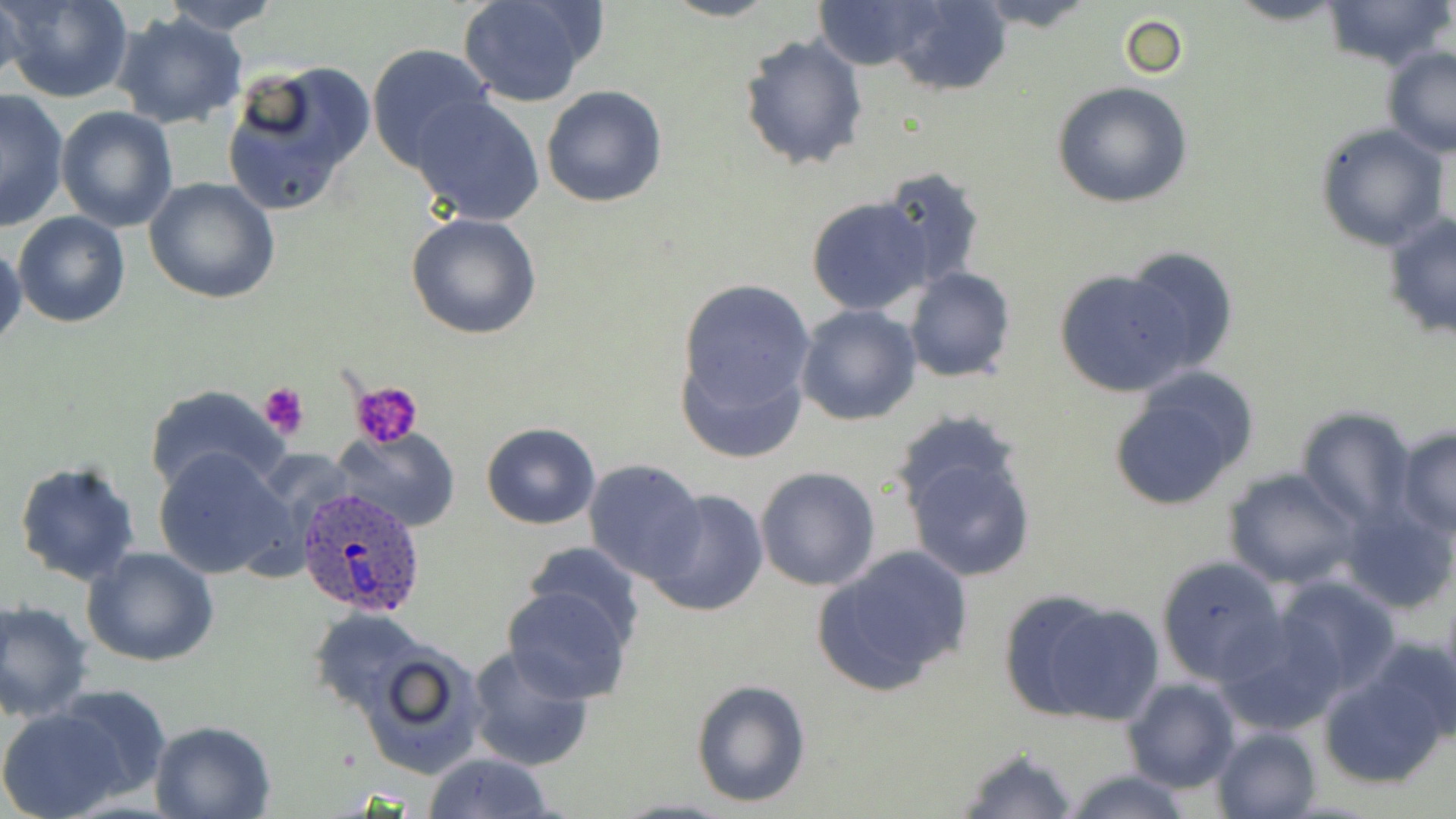 Approximate bounding boxes as (x1,y1)-(x2,y2) corner pairs in pixels. Uninfected red blood cell locations: (2,0)-(135,104), (159,0)-(283,34), (457,0)-(600,108), (662,0)-(779,22), (811,0)-(947,70), (887,0)-(1013,94), (971,0)-(1100,33), (1223,0)-(1350,28), (1319,0)-(1454,73), (0,3)-(29,91), (111,11)-(249,131), (1119,14)-(1188,80), (739,33)-(869,172), (366,43)-(494,171), (1381,46)-(1456,158), (220,61)-(374,217), (1051,82)-(1194,209), (542,85)-(668,207), (0,88)-(71,233), (410,96)-(544,226), (56,106)-(178,230), (1313,122)-(1450,251), (875,167)-(987,291), (144,177)-(281,304), (806,198)-(933,316), (13,211)-(129,328), (406,212)-(543,340), (1383,212)-(1456,342), (0,239)-(25,349), (1120,247)-(1242,373), (1054,265)-(1192,396), (904,268)-(1016,382), (674,276)-(817,446), (795,303)-(923,425), (1106,368)-(1260,514), (142,383)-(290,498), (1296,408)-(1417,528), (481,423)-(600,530), (330,427)-(461,533), (1395,427)-(1455,537), (898,432)-(1037,586), (152,446)-(296,581), (583,459)-(707,585), (12,461)-(143,586), (754,465)-(881,591), (1222,469)-(1363,589), (644,488)-(769,617), (1341,500)-(1456,614), (518,542)-(647,649), (809,545)-(974,697), (83,546)-(220,665), (1155,555)-(1288,686), (1273,574)-(1401,695), (502,582)-(634,704), (999,590)-(1163,727), (1,600)-(94,722), (309,607)-(433,714), (1215,615)-(1348,736), (1359,635)-(1456,755), (464,645)-(595,771), (357,646)-(487,778), (1316,663)-(1451,789), (1122,677)-(1241,794), (691,679)-(812,808), (51,683)-(174,800), (0,707)-(130,819), (149,719)-(277,818), (1210,725)-(1322,819), (955,746)-(1081,819), (423,751)-(556,819), (1060,767)-(1201,819), (609,798)-(740,819). Plasmodium ovale-infected red blood cell locations: (294,486)-(428,614). Platelet locations: (350,380)-(426,448), (257,382)-(310,441). Slide-level diagnosis: Plasmodium ovale. Captured at 1000x magnification. May-Grünwald-Giemsa-stained preparation. Image is 1456×819 pixels. One field of a larger specimen. Light microscopy. Thin blood smear.